Classify this cell by malaria status.
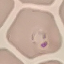

It is parasitized.

image type = cell patch, automatically extracted from a larger field of view and resized to 64 × 64 pixels
stain = Giemsa
preparation = thin blood smear
capture = smartphone camera at the microscope eyepiece